Identify the cell.
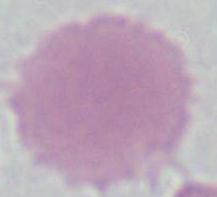

An erythrocyte.

Micrograph. Captured at 1000x magnification.